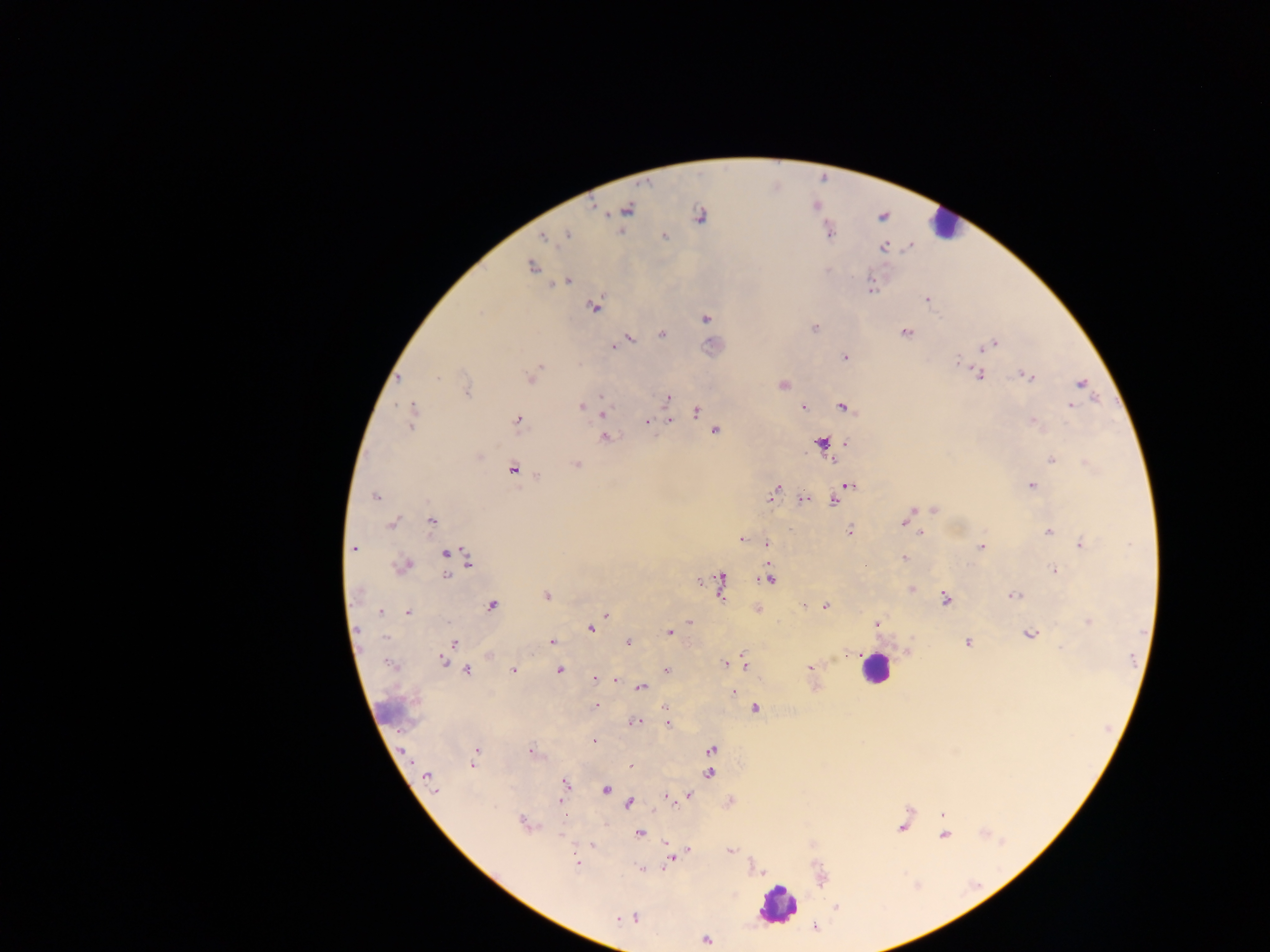
Approximate centers as [x, y] in pixels.
Summary:
  - Leukocyte locations: [943, 224], [874, 668], [604, 789], [777, 904]
  - Malaria parasite locations: [593, 207], [627, 210], [699, 216], [567, 234], [665, 236], [544, 237], [884, 248], [532, 267], [566, 281], [871, 288], [927, 300], [595, 307], [706, 319], [814, 327], [906, 332], [662, 334], [630, 339], [993, 343], [614, 347], [985, 347], [844, 357], [957, 361], [541, 366], [536, 371], [980, 375], [1027, 376], [398, 378], [436, 378], [531, 378], [1081, 384], [783, 385], [467, 392], [668, 397], [601, 398], [581, 406], [1072, 406], [803, 407], [843, 407], [413, 409], [696, 411], [603, 413], [412, 418], [518, 420], [669, 420], [646, 421], [1033, 423], [715, 431], [606, 437], [847, 443], [822, 444], [1052, 461], [576, 464], [1087, 464], [512, 469], [538, 476], [848, 485], [1032, 485], [773, 493], [841, 493], [376, 497], [802, 499], [833, 501], [934, 509], [431, 521], [902, 523], [392, 524], [849, 530], [920, 532], [1048, 532], [741, 539], [766, 542], [1082, 544], [981, 547], [354, 548], [446, 553], [904, 558], [469, 560], [404, 565], [1054, 570], [447, 574], [769, 579], [720, 584], [911, 588], [546, 595], [1014, 596], [945, 599], [492, 605], [804, 605], [825, 606], [381, 611], [407, 612], [606, 615], [690, 622], [1089, 622], [876, 624], [591, 628], [669, 633], [1030, 634], [552, 641], [628, 641], [453, 643], [968, 643], [849, 654], [443, 660], [744, 662], [725, 664], [810, 668], [513, 670], [560, 670], [667, 670], [467, 671], [595, 679], [615, 680], [642, 688], [733, 691], [596, 705], [666, 708], [755, 708], [634, 721], [667, 723], [594, 741], [711, 749], [476, 751], [530, 751], [473, 764], [630, 766], [709, 773], [428, 778], [566, 783], [689, 796], [668, 797], [560, 801], [629, 803], [942, 814], [523, 823], [902, 826], [640, 833], [944, 835], [730, 850], [672, 858], [576, 861], [641, 869], [837, 906], [634, 918], [617, 919], [706, 940]
  - Image size: 1270×952 pixels
  - Preparation: thick blood smear
  - Field of view: single
  - Capture: mobile-phone photograph through a microscope
  - Country: Ghana